Report the malaria status of this cell.
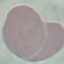
It is uninfected.

Giemsa-stained preparation. Automatically extracted cell patch, resized to 64 × 64 pixels. Thin smear of blood. Photographed with a smartphone camera at the microscope eyepiece.